Classify this cell by malaria status.
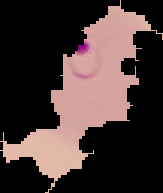

Parasitized.

image size = 163×193 pixels
image type = cell region segmented out of the field of view; surrounding area masked to black
preparation = thin blood smear